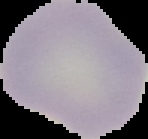

malaria status = uninfected
image type = segmented cell region on a black background
preparation = thin blood smear
image size = 148×139 pixels